Locate every Plasmodium falciparum parasite and give its life-cycle stage, and locate every leukocyte and any debris.
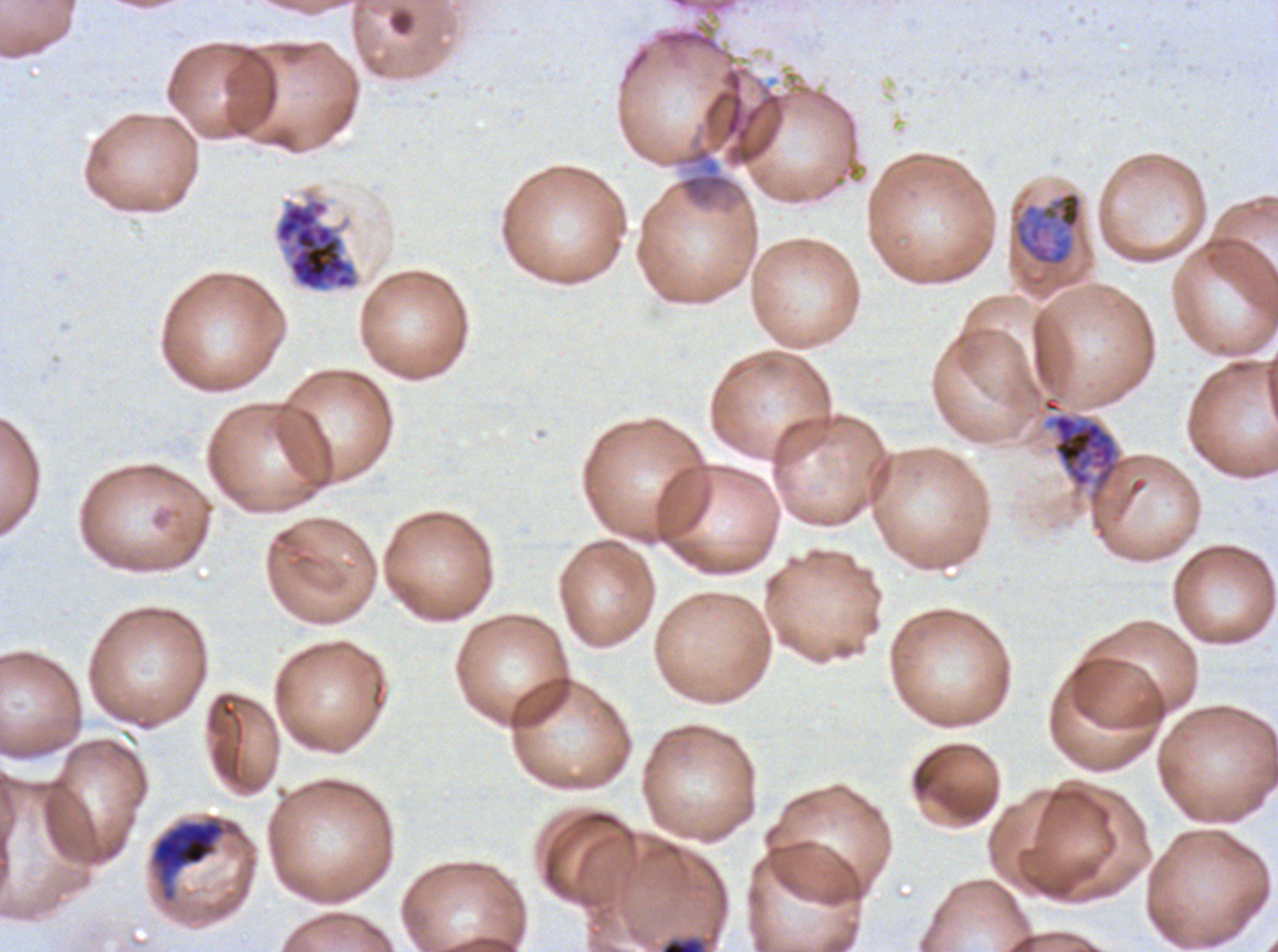

Approximate bounding boxes as [x1, y1, x2, y2] in pixels.
Late trophozoites: [1013, 190, 1083, 267].
Early schizonts: [1051, 412, 1118, 487], [150, 815, 240, 902].
Late schizonts: [275, 198, 359, 292].
Debris: [660, 937, 705, 951].
No rings, late-ring/early-trophozoite forms, mid trophozoites, segmenters, gametocytes, or leukocytes observed.

Summary:
  - Specimen: Plasmodium falciparum from a patient in The Gambia, cultured ex vivo for 24 to 48 hours
  - Image size: 1278×952 pixels
  - Stain: Giemsa
  - Life-cycle stages observed: late trophozoite, early schizont, late schizont
  - Field of view: one sub-image of a larger composite
  - Preparation: thin blood film